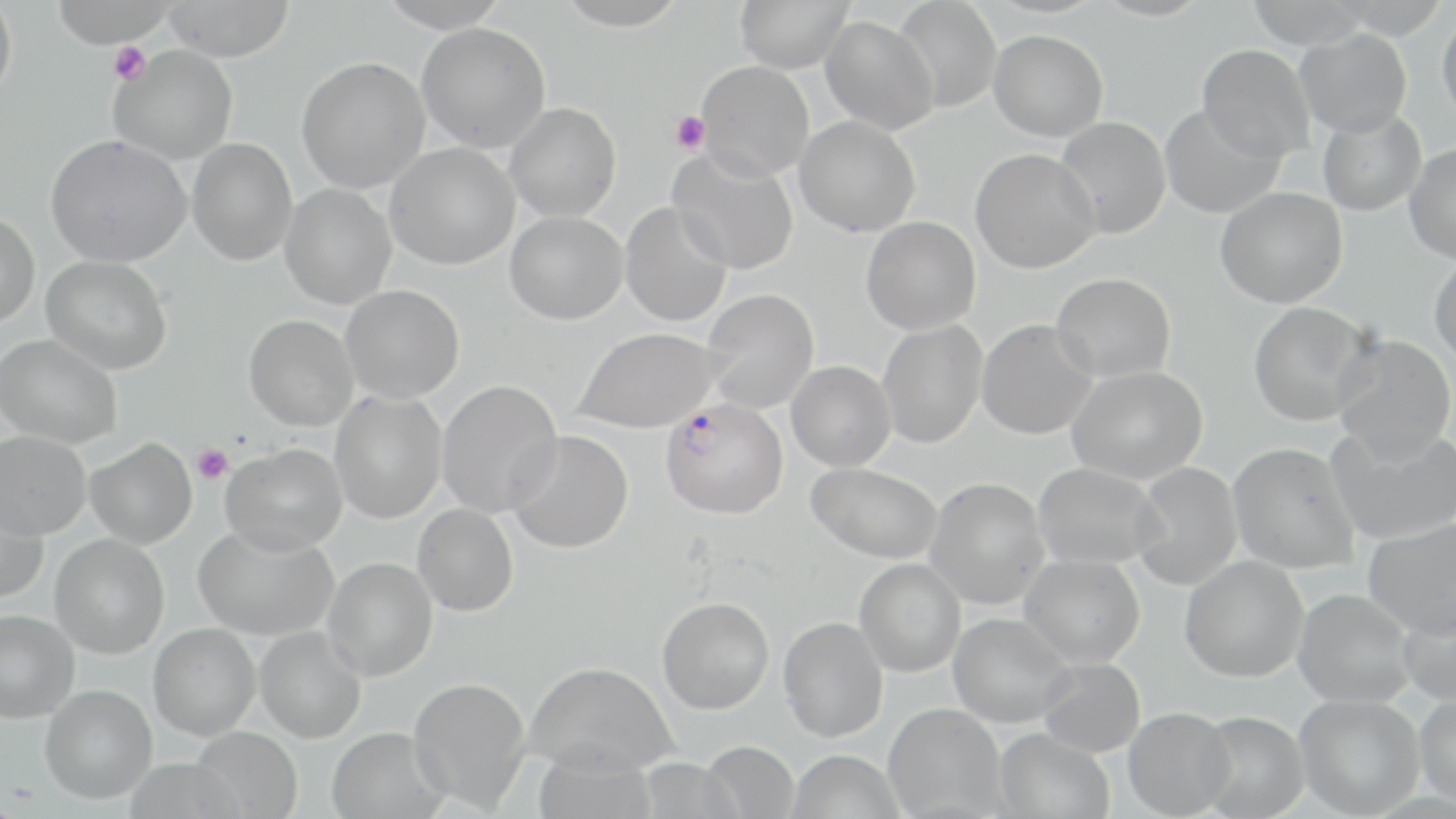 Approximate bounding boxes as [x1, y1, x2, y2] in pixels. Uninfected red blood cell locations: [0, 0, 18, 106], [49, 0, 180, 47], [375, 0, 513, 32], [552, 0, 690, 31], [735, 0, 853, 73], [1092, 0, 1212, 21], [1244, 0, 1372, 49], [162, 1, 295, 61], [891, 1, 1002, 113], [1437, 10, 1456, 124], [820, 16, 938, 134], [416, 22, 551, 153], [1294, 28, 1412, 137], [989, 30, 1108, 142], [1197, 44, 1315, 161], [108, 46, 238, 165], [296, 57, 430, 193], [696, 60, 814, 181], [504, 102, 621, 221], [1160, 103, 1285, 219], [1317, 110, 1426, 217], [795, 116, 921, 237], [1055, 116, 1171, 239], [45, 134, 191, 267], [187, 138, 298, 266], [385, 143, 519, 269], [1404, 143, 1456, 264], [667, 148, 799, 275], [970, 148, 1100, 273], [280, 184, 396, 309], [1215, 187, 1348, 308], [620, 202, 732, 327], [0, 211, 40, 329], [505, 211, 627, 324], [861, 217, 981, 335], [41, 255, 172, 374], [1429, 255, 1456, 366], [1051, 272, 1176, 382], [341, 285, 465, 404], [700, 289, 819, 414], [1248, 301, 1377, 426], [244, 315, 358, 431], [977, 319, 1098, 439], [877, 320, 987, 449], [574, 326, 721, 433], [0, 334, 122, 449], [1331, 335, 1455, 462], [786, 361, 896, 472], [1067, 366, 1207, 484], [436, 380, 563, 517], [329, 390, 447, 524], [1325, 424, 1456, 545], [507, 430, 634, 554], [0, 431, 91, 539], [85, 437, 197, 550], [1228, 442, 1361, 574], [221, 443, 347, 555], [806, 462, 942, 563], [1032, 462, 1165, 569], [1131, 462, 1242, 590], [925, 477, 1049, 610], [0, 493, 48, 604], [412, 503, 519, 617], [1362, 518, 1456, 638], [193, 523, 338, 641], [49, 535, 169, 659], [1020, 554, 1145, 667], [1180, 555, 1308, 682], [323, 557, 438, 681], [855, 558, 966, 677], [1293, 588, 1416, 707], [1397, 594, 1456, 707], [657, 597, 775, 714], [0, 610, 79, 723], [949, 612, 1075, 728], [778, 616, 888, 742], [148, 623, 260, 740], [255, 627, 366, 743], [1037, 657, 1146, 758], [525, 661, 678, 776], [408, 676, 531, 811], [40, 685, 157, 804], [1415, 693, 1456, 807], [1294, 694, 1425, 817], [883, 703, 1006, 819], [1123, 707, 1236, 818], [1196, 711, 1310, 819], [190, 726, 303, 819], [326, 726, 449, 819], [994, 728, 1116, 819], [701, 741, 799, 819], [532, 744, 659, 819], [786, 749, 905, 819], [634, 757, 745, 818], [125, 758, 244, 819]. Plasmodium falciparum-infected red blood cell locations: [660, 397, 788, 519]. Platelet locations: [109, 42, 150, 85], [670, 110, 710, 155], [192, 444, 233, 484]. Slide-level diagnosis: Plasmodium falciparum. Thin blood smear. May-Grünwald-Giemsa stain. 1000x magnification. Image is 1456×819 pixels. One field of a larger specimen. Light microscopy.